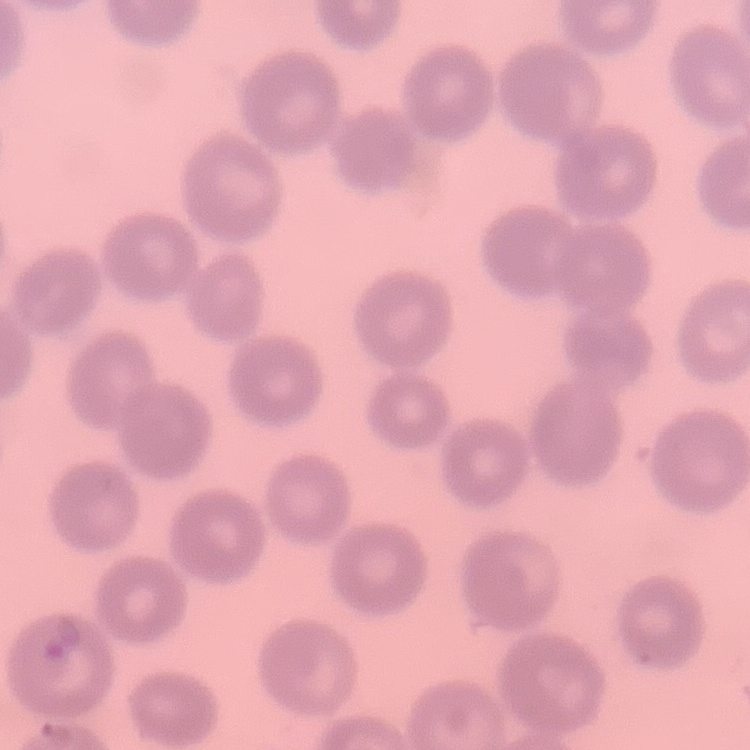 The red blood cells show no rouleaux formation. Square crop of a larger photomicrograph. Field's or Giemsa stain. Thin blood film.